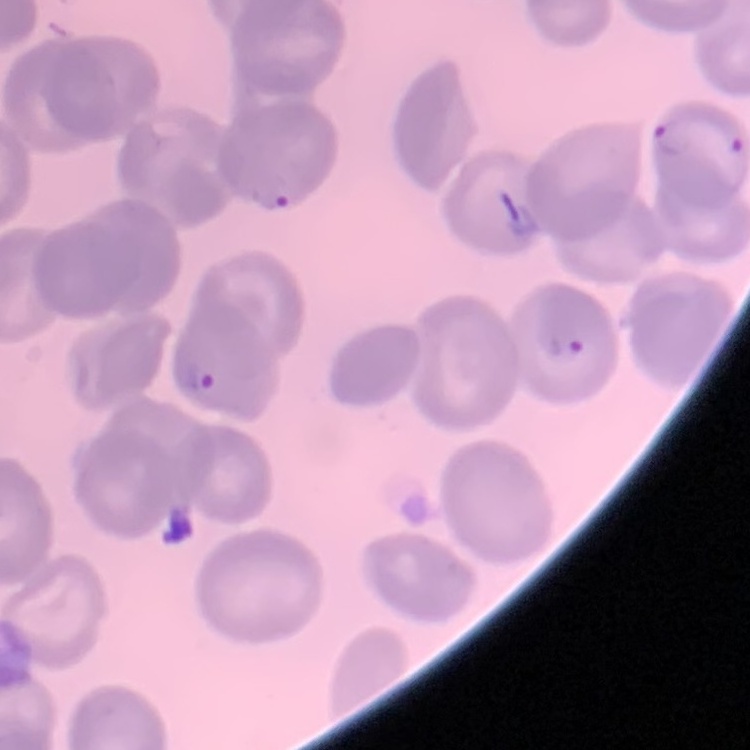
erythrocyte_morphology: no rouleaux formation
image_type: one tile cut from a larger photomicrograph
stain: Field's or Giemsa
preparation: thin blood film